State which parasite is depicted.
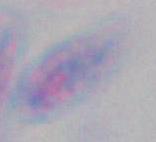
Toxoplasma gondii.

{
  "modality": "photomicrograph",
  "magnification": "1000x"
}